Locate every blood parasite and identify its species.
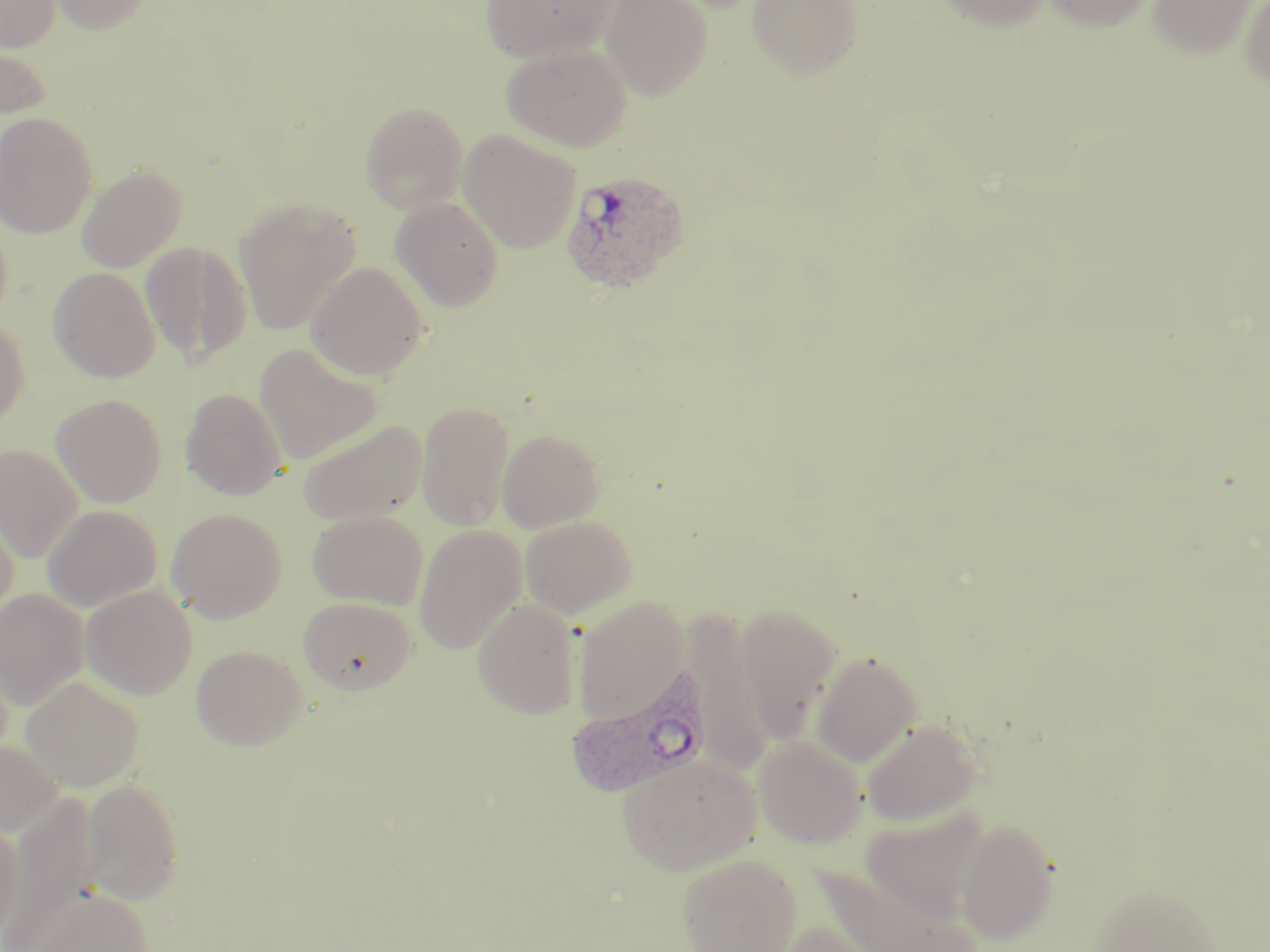

Approximate bounding boxes as (x1,y1)-(x2,y2) corner pairs in pixels.
Plasmodium ovale-infected red blood cells: (561,168)-(692,293), (567,669)-(712,798).
No Plasmodium falciparum, Plasmodium malariae, Plasmodium vivax, Babesia divergens, or Trypanosoma brucei observed.

Uninfected red blood cell locations: (0,0)-(61,52), (46,0)-(156,34), (481,0)-(619,62), (600,0)-(713,100), (747,0)-(863,81), (937,0)-(1052,31), (1041,0)-(1156,32), (1146,0)-(1258,60), (1239,0)-(1270,93), (0,37)-(52,125), (502,43)-(632,151), (360,102)-(468,213), (0,111)-(98,238), (458,130)-(581,253), (76,164)-(186,272), (233,197)-(361,336), (391,198)-(504,312), (140,241)-(252,366), (307,262)-(427,380), (49,267)-(159,382), (0,314)-(29,429), (253,343)-(384,465), (181,388)-(287,500), (50,394)-(167,507), (415,401)-(516,532), (297,419)-(428,526), (497,428)-(605,531), (0,443)-(83,562), (0,502)-(19,624), (41,505)-(162,612), (167,508)-(287,622), (307,510)-(428,609), (520,515)-(637,618), (413,524)-(526,654), (80,585)-(197,699), (0,588)-(89,710), (572,595)-(688,724), (298,596)-(417,694), (472,599)-(581,719), (736,603)-(841,742), (684,614)-(777,773), (191,645)-(308,750), (811,650)-(922,767), (20,676)-(144,791), (861,719)-(983,825), (753,735)-(868,849), (0,738)-(64,837), (616,752)-(761,875), (80,779)-(184,904), (4,794)-(101,950), (861,806)-(992,922), (0,820)-(25,945), (955,820)-(1060,945), (677,854)-(801,951), (811,861)-(978,950), (1088,882)-(1222,951), (21,884)-(155,951), (773,919)-(887,952). Slide-level diagnosis: Plasmodium ovale. Image is 1270×952 pixels. May-Grünwald-Giemsa-stained preparation. Thin blood film. Light microscopy. One field of a larger specimen. Captured at 1000x magnification.